Identify the blood parasite species.
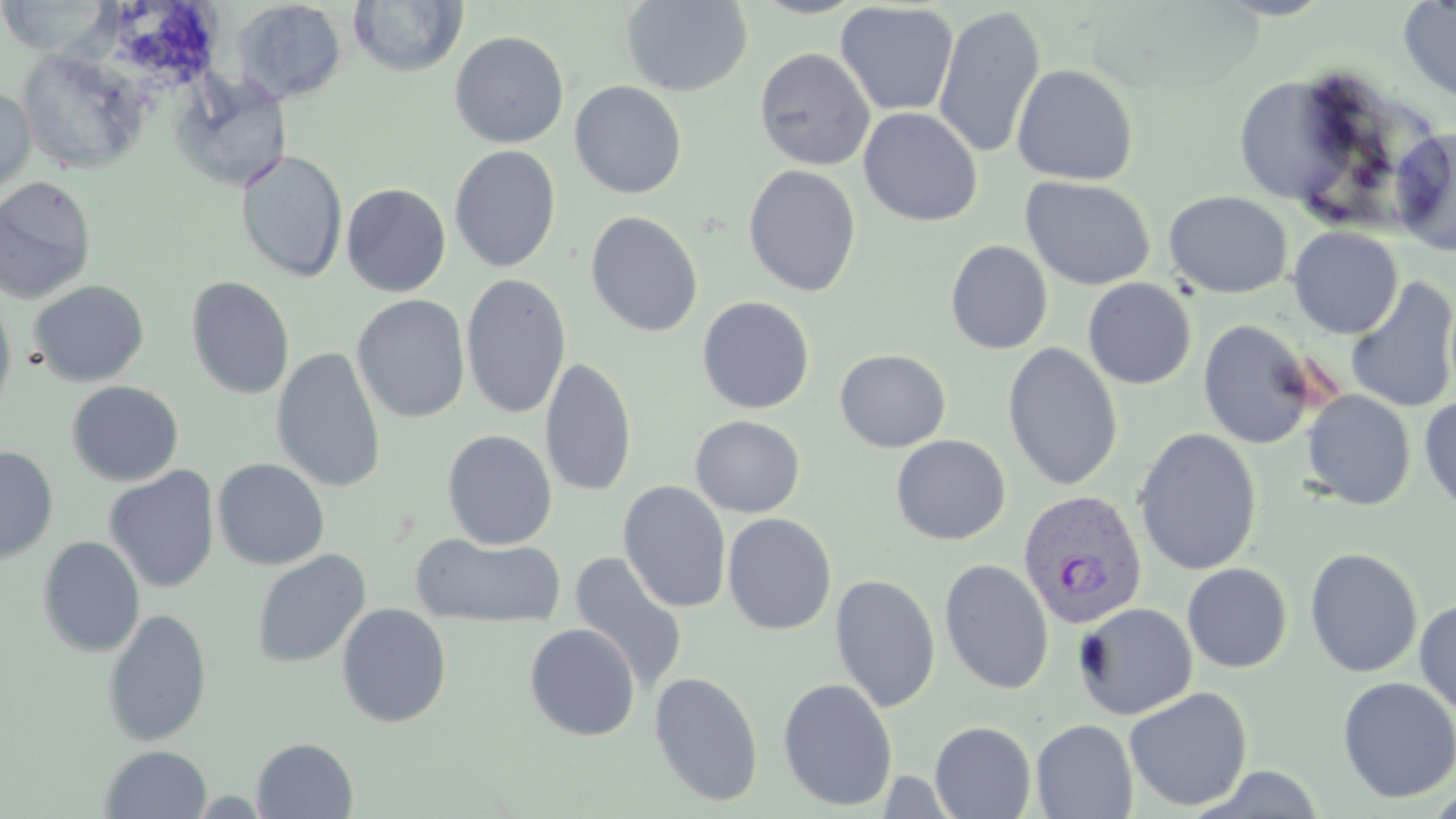
Plasmodium vivax.

preparation = thin blood film
stain = May-Grünwald-Giemsa
image size = 1456×819 pixels
uninfected red blood cell locations = approximate bounding boxes as named x1/y1/x2/y2 corners in pixels: (x1=348, y1=0, x2=467, y2=77), (x1=748, y1=0, x2=870, y2=19), (x1=1397, y1=0, x2=1456, y2=104), (x1=0, y1=1, x2=114, y2=57), (x1=231, y1=1, x2=348, y2=104), (x1=619, y1=1, x2=753, y2=97), (x1=835, y1=2, x2=959, y2=116), (x1=932, y1=6, x2=1046, y2=161), (x1=449, y1=30, x2=569, y2=148), (x1=17, y1=48, x2=148, y2=176), (x1=754, y1=48, x2=876, y2=171), (x1=891, y1=60, x2=1016, y2=202), (x1=1011, y1=64, x2=1138, y2=185), (x1=172, y1=75, x2=291, y2=191), (x1=569, y1=81, x2=687, y2=199), (x1=1239, y1=81, x2=1359, y2=210), (x1=0, y1=84, x2=36, y2=196), (x1=858, y1=107, x2=983, y2=226), (x1=1389, y1=128, x2=1456, y2=256), (x1=449, y1=145, x2=561, y2=273), (x1=236, y1=150, x2=348, y2=283), (x1=743, y1=164, x2=862, y2=297), (x1=1020, y1=175, x2=1156, y2=291), (x1=0, y1=176, x2=97, y2=304), (x1=341, y1=183, x2=451, y2=297), (x1=1164, y1=191, x2=1292, y2=299), (x1=585, y1=210, x2=703, y2=338), (x1=1288, y1=226, x2=1403, y2=339), (x1=945, y1=240, x2=1053, y2=354), (x1=460, y1=272, x2=572, y2=420), (x1=185, y1=276, x2=294, y2=399), (x1=1345, y1=276, x2=1456, y2=414), (x1=1083, y1=278, x2=1197, y2=389), (x1=28, y1=280, x2=149, y2=387), (x1=0, y1=289, x2=17, y2=422), (x1=352, y1=294, x2=470, y2=423), (x1=697, y1=296, x2=815, y2=414), (x1=1197, y1=318, x2=1321, y2=450), (x1=1002, y1=342, x2=1124, y2=492), (x1=271, y1=346, x2=387, y2=493), (x1=835, y1=349, x2=951, y2=452), (x1=540, y1=356, x2=637, y2=498), (x1=67, y1=381, x2=184, y2=486), (x1=1301, y1=390, x2=1416, y2=510), (x1=1419, y1=396, x2=1456, y2=517), (x1=690, y1=415, x2=805, y2=518), (x1=1133, y1=428, x2=1263, y2=576), (x1=441, y1=429, x2=557, y2=550), (x1=891, y1=434, x2=1011, y2=545), (x1=0, y1=446, x2=58, y2=565), (x1=212, y1=458, x2=330, y2=571), (x1=103, y1=465, x2=220, y2=593), (x1=618, y1=481, x2=732, y2=613), (x1=722, y1=512, x2=837, y2=635), (x1=411, y1=533, x2=564, y2=628), (x1=37, y1=536, x2=145, y2=657), (x1=1304, y1=547, x2=1423, y2=677), (x1=251, y1=549, x2=371, y2=669), (x1=568, y1=552, x2=688, y2=695), (x1=938, y1=558, x2=1054, y2=695), (x1=1182, y1=563, x2=1292, y2=673), (x1=829, y1=573, x2=941, y2=712), (x1=1414, y1=597, x2=1456, y2=717), (x1=1073, y1=602, x2=1197, y2=720), (x1=336, y1=603, x2=452, y2=728), (x1=101, y1=608, x2=213, y2=747), (x1=524, y1=623, x2=640, y2=741), (x1=648, y1=671, x2=765, y2=807), (x1=1337, y1=676, x2=1456, y2=804), (x1=777, y1=678, x2=898, y2=811), (x1=1123, y1=687, x2=1253, y2=812), (x1=1030, y1=718, x2=1138, y2=819), (x1=929, y1=721, x2=1037, y2=818), (x1=251, y1=737, x2=358, y2=818), (x1=100, y1=744, x2=212, y2=818)
Plasmodium vivax-infected red blood cell locations = approximate bounding boxes as named x1/y1/x2/y2 corners in pixels: (x1=1017, y1=489, x2=1147, y2=633)
modality = light microscopy
field of view = one of a larger specimen
magnification = 1000x